Locate every malaria parasite.
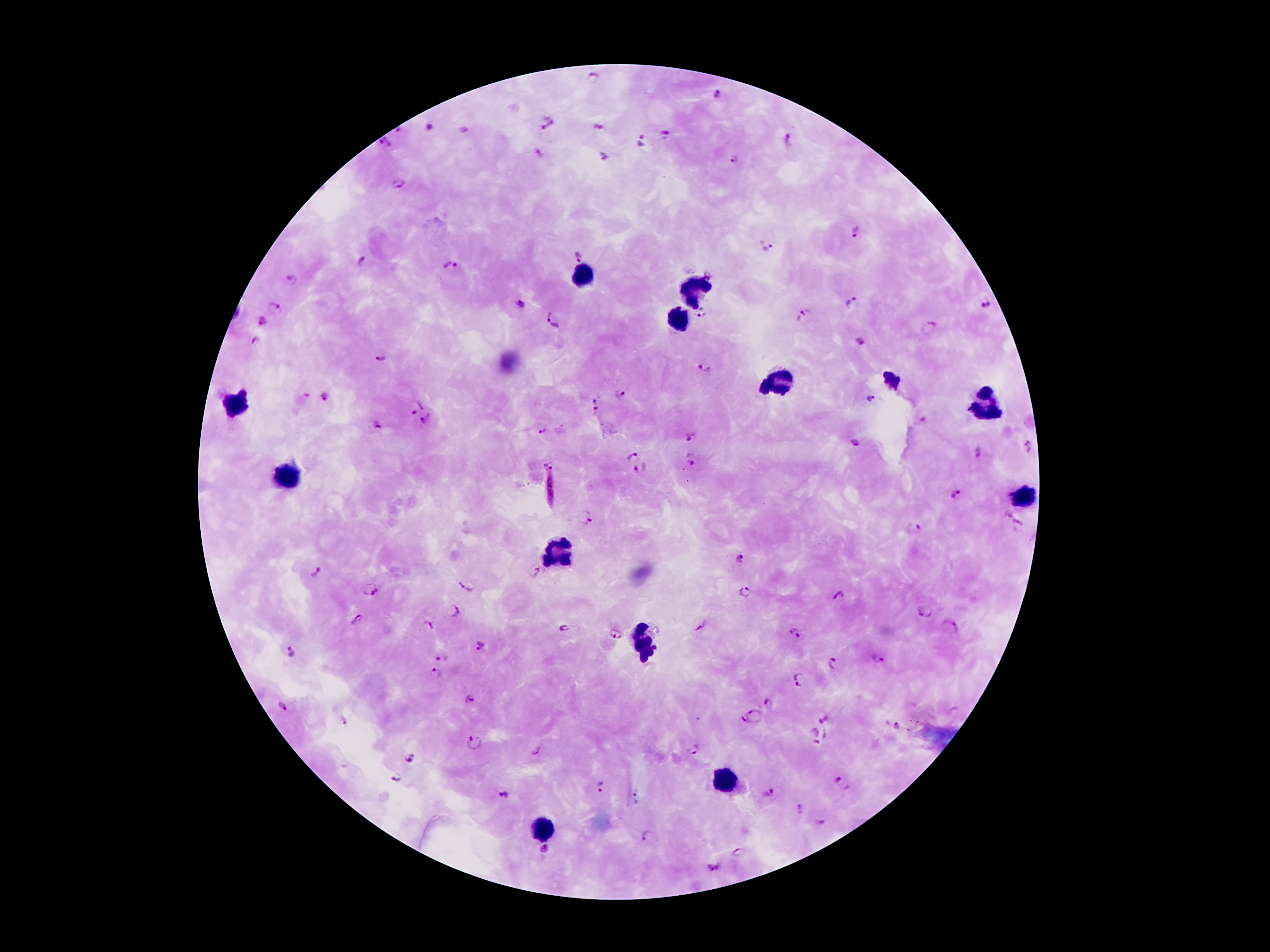

Approximate centers as [x, y] in pixels.
Malaria parasites: [593, 77], [715, 95], [548, 123], [430, 126], [601, 126], [665, 134], [790, 139], [641, 140], [385, 142], [539, 151], [601, 155], [735, 159], [398, 183], [855, 231], [768, 247], [576, 256], [362, 260], [452, 266], [291, 279], [852, 301], [520, 302], [984, 304], [275, 308], [700, 315], [803, 316], [555, 319], [262, 321], [931, 326], [861, 342], [256, 343], [384, 355], [704, 368], [325, 396], [621, 396], [871, 399], [416, 407], [595, 409], [427, 420], [924, 421], [375, 425], [541, 429], [690, 434], [855, 443], [1028, 445], [631, 451], [976, 452], [693, 462], [548, 464], [639, 469], [548, 490], [958, 494], [1007, 514], [585, 518], [1019, 526], [916, 527], [741, 559], [535, 570], [316, 572], [466, 586], [372, 589], [744, 592], [840, 595], [456, 611], [923, 611], [356, 619], [429, 624], [703, 625], [951, 627], [564, 629], [797, 633], [613, 634], [479, 646], [290, 652], [441, 657], [879, 659], [833, 665], [436, 674], [801, 681], [471, 698], [770, 703], [284, 708], [754, 716], [827, 719], [345, 723], [895, 727], [814, 731], [822, 741], [472, 742], [694, 749], [536, 752], [407, 758], [398, 778], [842, 782], [600, 788], [769, 793], [504, 794], [800, 810], [821, 823], [651, 838], [544, 849], [740, 852], [715, 867].

leukocyte locations = [586, 274], [694, 291], [680, 321], [779, 383], [238, 405], [982, 407], [290, 478], [1028, 497], [559, 551], [643, 642], [723, 781], [545, 830]
preparation = thick blood smear
stain = Giemsa
magnification = 100x
capture = smartphone camera through the microscope eyepiece
image size = 1270×952 pixels
field of view = one from this slide
patient malaria status = infected with Plasmodium falciparum